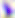

identification: Toxoplasma gondii
magnification: 400x
modality: micrograph